Locate and identify every blood parasite.
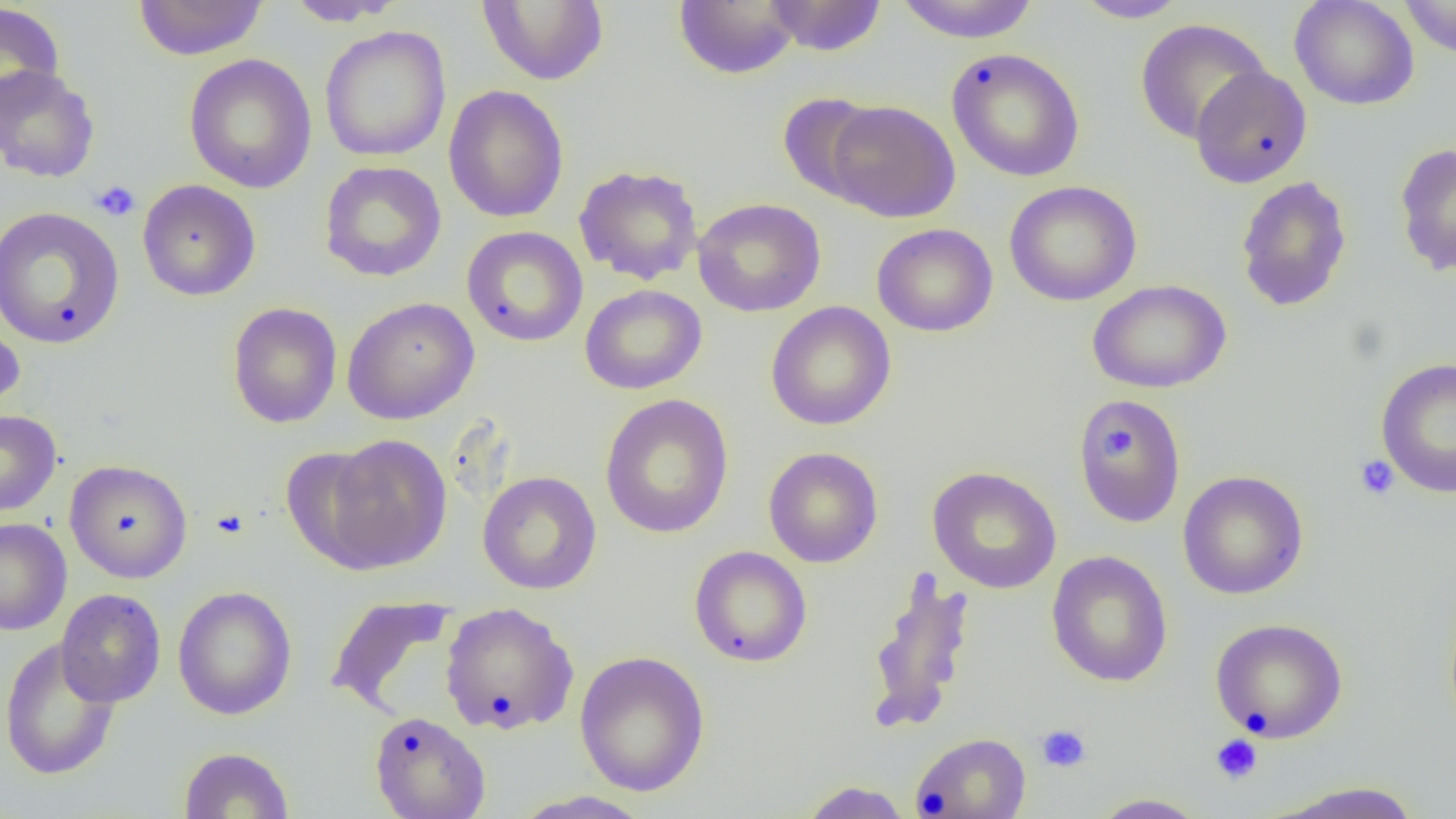

No blood parasites seen.

Summary:
  - Coordinate format: approximate bounding boxes as (x1, y1, x2, y2) in pixels
  - Platelet locations: (91, 180, 141, 222), (1100, 428, 1132, 457), (1355, 455, 1399, 500), (210, 507, 250, 541), (1035, 724, 1092, 773), (1210, 734, 1263, 784)
  - Uninfected red blood cell locations: (132, 0, 269, 60), (282, 0, 407, 26), (476, 0, 610, 86), (673, 0, 802, 80), (763, 0, 888, 56), (893, 0, 1041, 43), (1071, 0, 1192, 23), (1289, 0, 1420, 110), (1398, 0, 1456, 59), (0, 2, 66, 120), (1134, 17, 1270, 144), (319, 26, 451, 162), (946, 48, 1085, 182), (184, 53, 317, 193), (0, 65, 100, 183), (1190, 65, 1312, 188), (443, 85, 569, 223), (777, 92, 886, 204), (826, 99, 960, 222), (1394, 143, 1456, 277), (319, 160, 447, 282), (573, 164, 704, 286), (1235, 175, 1352, 313), (137, 179, 261, 301), (1004, 181, 1142, 306), (692, 197, 826, 317), (0, 206, 125, 350), (872, 223, 999, 337), (461, 226, 588, 347), (1087, 280, 1231, 393), (579, 284, 707, 395), (342, 297, 480, 424), (227, 301, 342, 428), (765, 301, 896, 431), (0, 315, 26, 416), (1375, 358, 1456, 499), (599, 393, 735, 539), (1072, 395, 1187, 527), (0, 410, 61, 516), (318, 434, 451, 574), (278, 446, 395, 573), (764, 447, 883, 568), (64, 459, 193, 583), (927, 466, 1062, 594), (1177, 470, 1309, 600), (478, 471, 602, 594), (0, 518, 72, 635), (689, 546, 812, 668), (1047, 550, 1173, 687), (864, 571, 976, 734), (172, 585, 298, 720), (56, 588, 166, 707), (325, 595, 456, 717), (439, 601, 579, 736), (1210, 618, 1348, 742), (0, 637, 120, 780), (574, 650, 710, 797), (369, 711, 491, 819), (910, 732, 1031, 818), (178, 746, 294, 818), (797, 780, 913, 818), (1267, 781, 1424, 818), (509, 791, 656, 819), (1089, 793, 1211, 818)
  - Slide-level diagnosis: negative for blood parasites
  - Magnification: 1000x
  - Preparation: thin blood film
  - Modality: light microscopy
  - Image size: 1456×819 pixels
  - Field of view: single